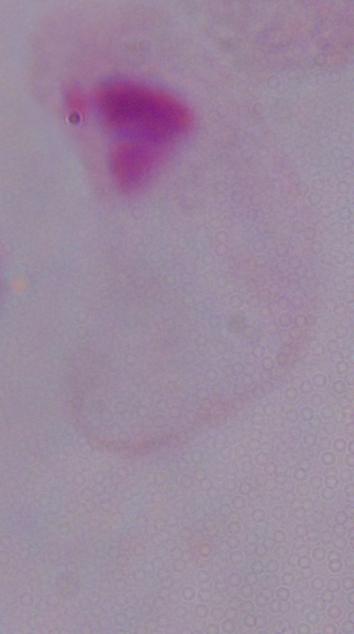
Summary:
  - Modality: photomicrograph
  - Identification: trichomonad
  - Magnification: 1000x